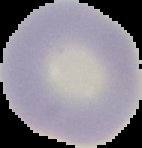 The area outside the segmented cell region is set to black. Image is 142×148 pixels. From a thin blood film. Result: no malaria parasites seen.